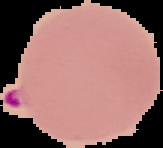
Summary:
  - Malaria status: parasitized
  - Preparation: thin blood film
  - Image size: 163×148 pixels
  - Image type: segmented cell region with the area outside set to black